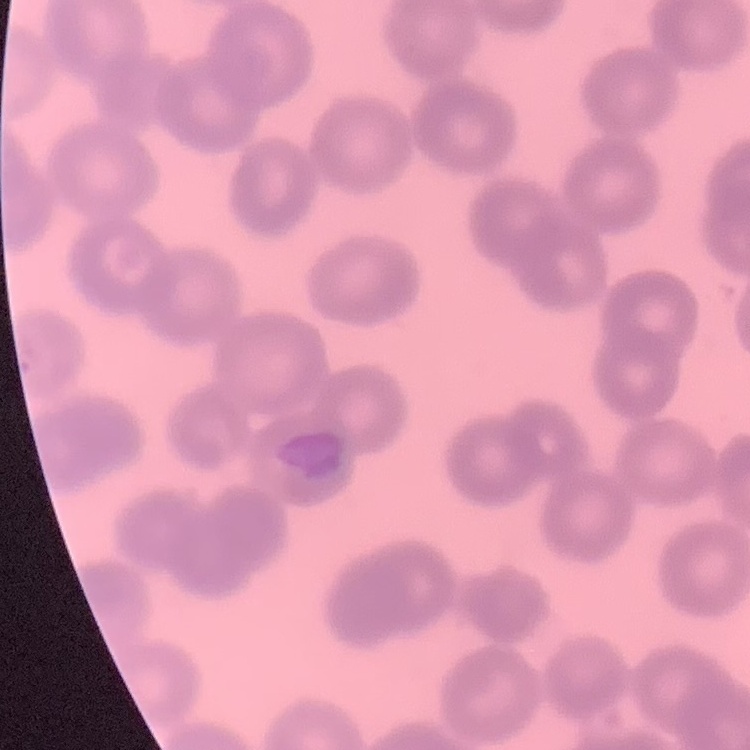

red blood cell morphology = no rouleaux formation
preparation = thin blood film
image type = one tile cut from a larger photomicrograph
stain = Field's or Giemsa